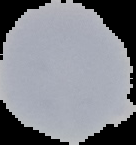

Summary:
  - Malaria status: uninfected
  - Image size: 136×145 pixels
  - Image type: cell region segmented out of the field of view; surrounding area masked to black
  - Preparation: thin blood smear